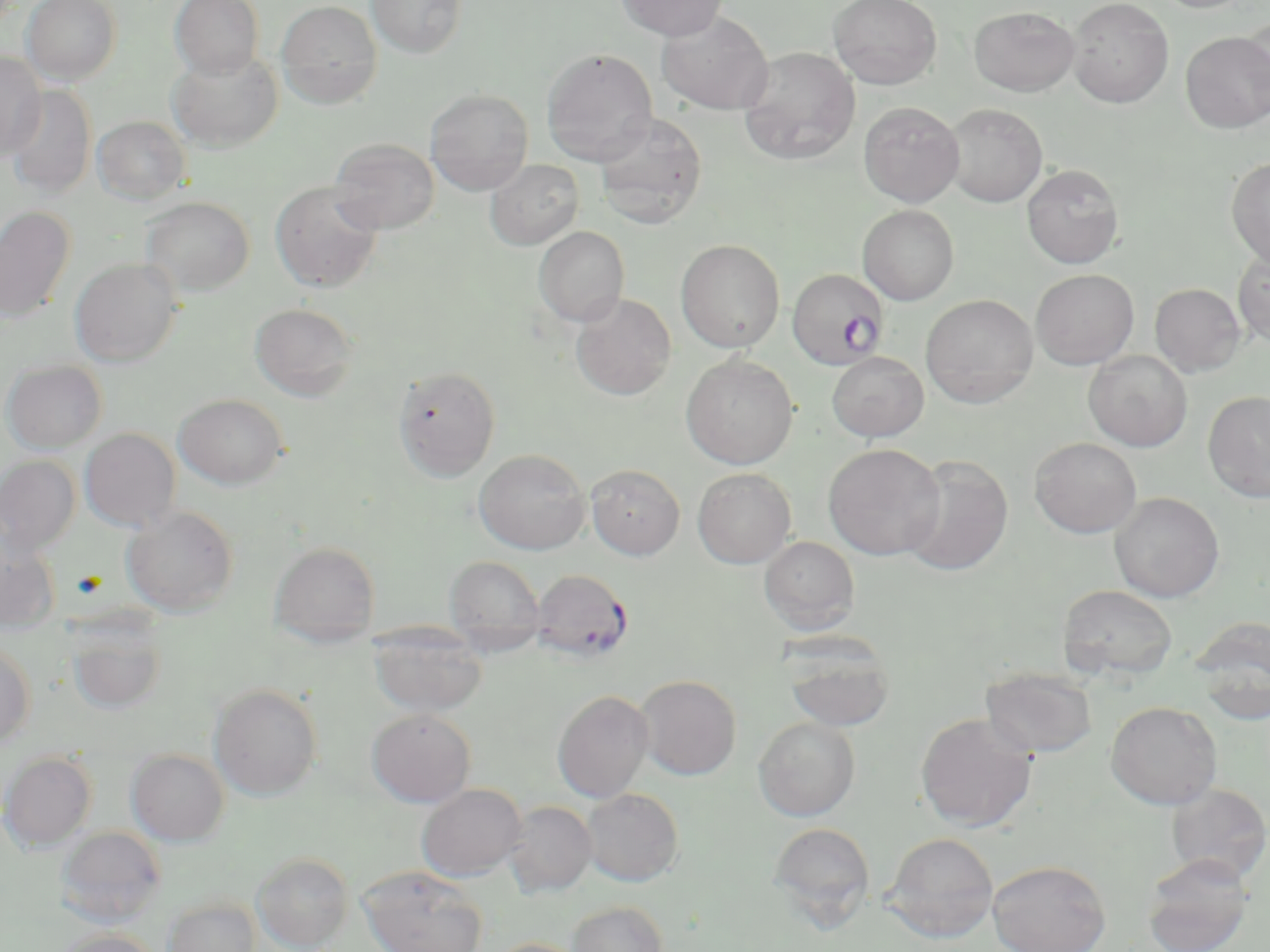

Approximate bounding boxes as named x1/y1/x2/y2 corners in pixels. Plasmodium falciparum-infected red blood cell locations: (x1=786, y1=267, x2=889, y2=369), (x1=531, y1=568, x2=633, y2=663). Uninfected red blood cell locations: (x1=21, y1=0, x2=121, y2=85), (x1=170, y1=0, x2=264, y2=80), (x1=276, y1=0, x2=383, y2=108), (x1=366, y1=0, x2=467, y2=59), (x1=616, y1=0, x2=728, y2=41), (x1=828, y1=0, x2=943, y2=90), (x1=1067, y1=0, x2=1174, y2=108), (x1=1152, y1=0, x2=1255, y2=13), (x1=968, y1=6, x2=1081, y2=96), (x1=657, y1=9, x2=774, y2=115), (x1=1244, y1=15, x2=1270, y2=118), (x1=1180, y1=31, x2=1270, y2=133), (x1=737, y1=47, x2=860, y2=165), (x1=541, y1=48, x2=658, y2=165), (x1=166, y1=49, x2=284, y2=152), (x1=0, y1=51, x2=47, y2=161), (x1=5, y1=85, x2=97, y2=199), (x1=425, y1=89, x2=533, y2=195), (x1=858, y1=101, x2=964, y2=207), (x1=943, y1=103, x2=1048, y2=206), (x1=593, y1=112, x2=707, y2=230), (x1=92, y1=116, x2=190, y2=204), (x1=329, y1=137, x2=439, y2=234), (x1=1226, y1=157, x2=1270, y2=269), (x1=485, y1=159, x2=584, y2=250), (x1=1022, y1=164, x2=1125, y2=268), (x1=270, y1=180, x2=384, y2=293), (x1=141, y1=196, x2=254, y2=297), (x1=857, y1=204, x2=959, y2=305), (x1=0, y1=206, x2=76, y2=323), (x1=533, y1=226, x2=630, y2=327), (x1=676, y1=239, x2=785, y2=353), (x1=1233, y1=248, x2=1270, y2=348), (x1=69, y1=258, x2=183, y2=367), (x1=1030, y1=269, x2=1139, y2=370), (x1=1150, y1=283, x2=1246, y2=377), (x1=571, y1=293, x2=676, y2=400), (x1=920, y1=294, x2=1039, y2=407), (x1=250, y1=302, x2=360, y2=401), (x1=1083, y1=350, x2=1192, y2=451), (x1=827, y1=352, x2=929, y2=442), (x1=681, y1=354, x2=798, y2=469), (x1=2, y1=359, x2=107, y2=453), (x1=393, y1=365, x2=501, y2=482), (x1=1203, y1=390, x2=1270, y2=504), (x1=174, y1=393, x2=288, y2=489), (x1=79, y1=428, x2=181, y2=532), (x1=1030, y1=437, x2=1142, y2=538), (x1=823, y1=443, x2=945, y2=560), (x1=474, y1=449, x2=590, y2=554), (x1=0, y1=455, x2=81, y2=553), (x1=899, y1=455, x2=1014, y2=576), (x1=585, y1=464, x2=685, y2=559), (x1=692, y1=468, x2=796, y2=568), (x1=1109, y1=492, x2=1225, y2=602), (x1=121, y1=505, x2=239, y2=616), (x1=0, y1=533, x2=61, y2=629), (x1=758, y1=535, x2=860, y2=636), (x1=269, y1=541, x2=380, y2=648), (x1=444, y1=556, x2=545, y2=654), (x1=1058, y1=584, x2=1178, y2=682), (x1=1191, y1=617, x2=1270, y2=721), (x1=66, y1=619, x2=168, y2=715), (x1=369, y1=622, x2=488, y2=718), (x1=781, y1=630, x2=896, y2=731), (x1=0, y1=640, x2=35, y2=748), (x1=980, y1=666, x2=1098, y2=758), (x1=635, y1=674, x2=741, y2=780), (x1=208, y1=683, x2=323, y2=801), (x1=552, y1=690, x2=654, y2=803), (x1=1106, y1=701, x2=1223, y2=810), (x1=366, y1=709, x2=476, y2=807), (x1=915, y1=712, x2=1037, y2=832), (x1=754, y1=716, x2=860, y2=821), (x1=126, y1=748, x2=230, y2=846), (x1=1, y1=751, x2=97, y2=851), (x1=416, y1=783, x2=527, y2=881), (x1=1165, y1=783, x2=1270, y2=886), (x1=581, y1=788, x2=683, y2=886), (x1=503, y1=801, x2=597, y2=897), (x1=767, y1=822, x2=875, y2=928), (x1=54, y1=826, x2=166, y2=926), (x1=885, y1=832, x2=998, y2=942), (x1=252, y1=851, x2=354, y2=952), (x1=1141, y1=853, x2=1253, y2=952), (x1=988, y1=860, x2=1110, y2=952), (x1=358, y1=866, x2=489, y2=952), (x1=163, y1=897, x2=261, y2=952), (x1=566, y1=900, x2=669, y2=952), (x1=54, y1=929, x2=163, y2=952), (x1=488, y1=937, x2=588, y2=952). Slide-level diagnosis: Plasmodium falciparum. Thin blood film. 1000x magnification. Optical microscopy. One field of a larger specimen. Image is 1270×952 pixels. May-Grünwald-Giemsa stain.